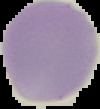

{
  "image_size": "100×109 pixels",
  "image_type": "segmented cell region with the area outside set to black",
  "result": "no Plasmodium parasites detected",
  "preparation": "thin blood smear"
}